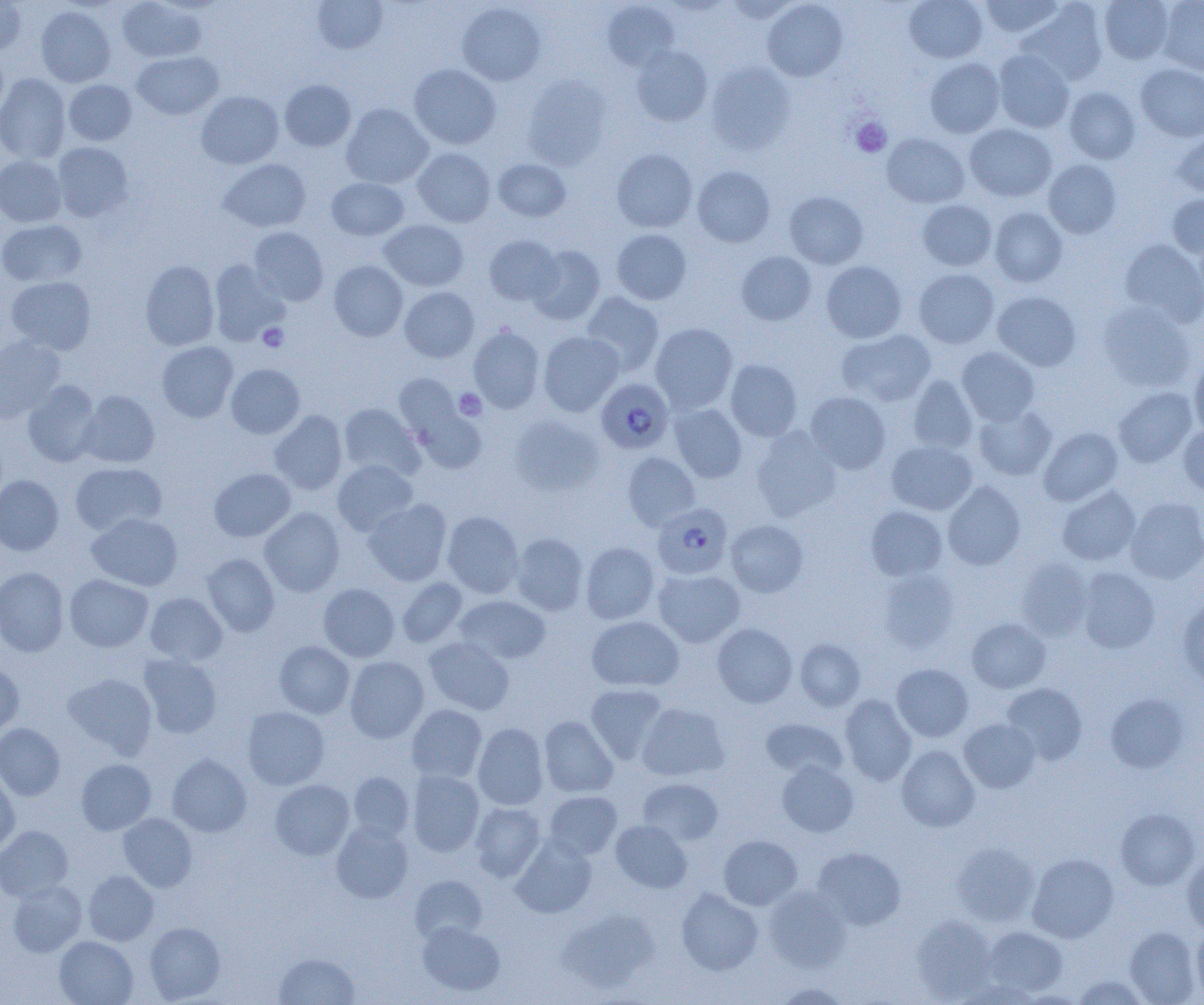

slide-level diagnosis = Plasmodium falciparum
field of view = single
magnification = 1000x
uninfected red blood cell locations = approximate bounding boxes as (x1, y1, x2, y2) in pixels: (0, 0, 27, 56), (116, 0, 206, 63), (904, 0, 987, 63), (978, 0, 1066, 40), (1099, 0, 1174, 64), (1157, 0, 1204, 77), (312, 1, 388, 54), (602, 1, 680, 71), (725, 1, 801, 23), (762, 1, 848, 82), (1019, 1, 1108, 86), (456, 3, 546, 86), (36, 6, 115, 87), (630, 45, 713, 126), (0, 49, 8, 121), (993, 49, 1074, 133), (132, 51, 223, 120), (925, 58, 1005, 138), (706, 62, 796, 154), (1136, 63, 1204, 142), (408, 64, 501, 149), (0, 74, 71, 163), (522, 75, 612, 170), (63, 79, 137, 145), (279, 80, 356, 151), (1064, 87, 1140, 164), (196, 91, 284, 169), (341, 103, 433, 189), (964, 123, 1057, 202), (1172, 130, 1204, 198), (882, 133, 969, 208), (52, 142, 134, 222), (412, 148, 496, 227), (611, 148, 697, 232), (0, 155, 66, 228), (219, 159, 311, 232), (493, 159, 571, 221), (1043, 159, 1122, 239), (692, 166, 775, 247), (326, 177, 409, 240), (785, 192, 868, 269), (1166, 194, 1204, 258), (917, 199, 997, 271), (989, 207, 1067, 287), (0, 219, 87, 287), (378, 219, 469, 291), (248, 227, 328, 306), (611, 229, 691, 305), (484, 234, 563, 306), (1119, 238, 1204, 326), (527, 245, 605, 325), (736, 251, 817, 325), (209, 259, 289, 346), (140, 260, 220, 350), (329, 260, 408, 341), (821, 260, 906, 343), (913, 269, 999, 349), (5, 276, 96, 355), (399, 287, 479, 362), (992, 290, 1082, 371), (581, 292, 664, 376), (1097, 300, 1196, 392), (650, 323, 738, 413), (469, 326, 545, 413), (836, 329, 936, 407), (538, 331, 624, 416), (0, 335, 66, 422), (156, 341, 238, 422), (957, 347, 1040, 425), (1190, 358, 1204, 438), (725, 359, 802, 441), (226, 364, 305, 439), (907, 375, 978, 454), (395, 378, 485, 467), (22, 380, 102, 467), (1113, 387, 1197, 468), (78, 390, 160, 468), (805, 391, 891, 474), (339, 403, 424, 481), (670, 403, 747, 482), (973, 405, 1057, 481), (269, 410, 348, 495), (509, 415, 603, 497), (1178, 424, 1204, 496), (751, 427, 841, 521), (1039, 427, 1123, 506), (885, 441, 977, 516), (623, 452, 700, 530), (332, 459, 418, 535), (69, 462, 167, 536), (209, 468, 296, 542), (0, 475, 63, 555), (943, 481, 1025, 570), (1057, 486, 1141, 566), (1125, 497, 1204, 584), (363, 499, 452, 586), (865, 505, 948, 581), (259, 507, 345, 596), (442, 511, 524, 598), (86, 512, 183, 591), (726, 519, 808, 597), (509, 532, 589, 616), (580, 542, 660, 624), (201, 553, 280, 637), (1016, 558, 1093, 640), (0, 567, 69, 656), (1076, 567, 1160, 653), (653, 569, 745, 647), (878, 569, 960, 652), (64, 574, 153, 652), (396, 577, 468, 648), (318, 583, 399, 662), (144, 592, 227, 666), (454, 595, 551, 664), (1177, 597, 1204, 687), (587, 616, 684, 691), (967, 617, 1051, 693), (712, 623, 797, 708), (424, 636, 515, 715), (794, 638, 865, 711), (274, 641, 355, 718), (139, 653, 222, 738), (345, 656, 429, 743), (0, 662, 24, 735), (892, 663, 973, 741), (63, 672, 157, 758), (1001, 682, 1088, 765), (585, 683, 668, 764), (1105, 693, 1190, 773), (839, 694, 917, 786), (637, 702, 729, 781), (407, 704, 487, 783), (242, 706, 329, 790), (539, 716, 618, 798), (759, 717, 848, 781), (959, 718, 1040, 792), (473, 722, 548, 810), (0, 723, 65, 800), (896, 745, 980, 832), (167, 754, 252, 837), (76, 758, 156, 835), (777, 760, 858, 837), (407, 770, 484, 857), (347, 771, 414, 841), (0, 775, 20, 853), (269, 778, 355, 860), (637, 778, 723, 846), (544, 791, 622, 860), (470, 802, 545, 881), (1115, 808, 1200, 890), (119, 813, 198, 892), (331, 820, 414, 903), (611, 820, 692, 893), (0, 826, 73, 902), (719, 835, 802, 910), (511, 837, 596, 918), (951, 842, 1039, 927), (812, 847, 906, 930), (1027, 853, 1118, 943), (1182, 854, 1204, 936), (83, 870, 159, 945), (410, 875, 487, 944), (7, 880, 87, 956), (764, 886, 850, 972), (676, 887, 763, 975), (558, 908, 660, 993), (911, 914, 997, 1001), (417, 920, 505, 997), (144, 922, 225, 1003), (983, 926, 1067, 996), (1125, 926, 1201, 1004), (1192, 928, 1204, 1000), (54, 936, 138, 1005), (273, 952, 361, 1005), (1072, 975, 1151, 1004), (771, 983, 854, 1004)
image size = 1204×1005 pixels
preparation = thin blood smear
modality = optical microscopy
platelet locations = approximate bounding boxes as (x1, y1, x2, y2) in pixels: (851, 117, 891, 157), (258, 322, 289, 352), (454, 388, 487, 420)
Plasmodium falciparum-infected red blood cell locations = approximate bounding boxes as (x1, y1, x2, y2) in pixels: (596, 378, 674, 454), (653, 503, 733, 579)